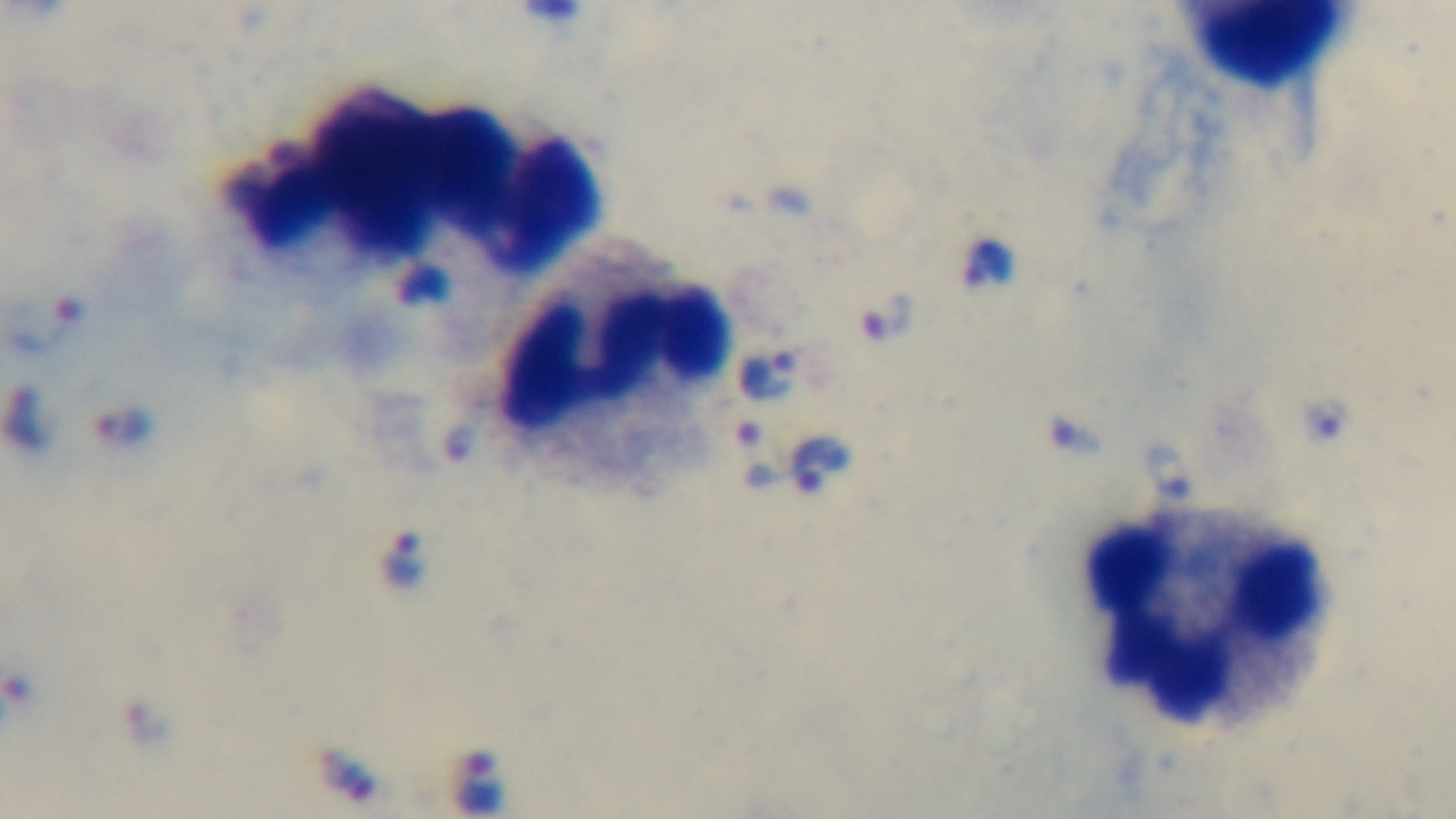

Summary:
  - Preparation: thick
  - Field of view: one from the slide
  - Stain: Giemsa
  - Modality: light microscopy
  - Objective: 100x oil immersion
  - Malaria status: positive
  - Capture: mounted 4K digital camera